Report the malaria status of this cell.
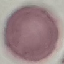
It is uninfected.

Summary:
  - Image type: automatically extracted cell patch, resized to 64 × 64 pixels
  - Preparation: thin smear
  - Stain: Giemsa
  - Capture: smartphone camera at the microscope eyepiece